State the preparation type.
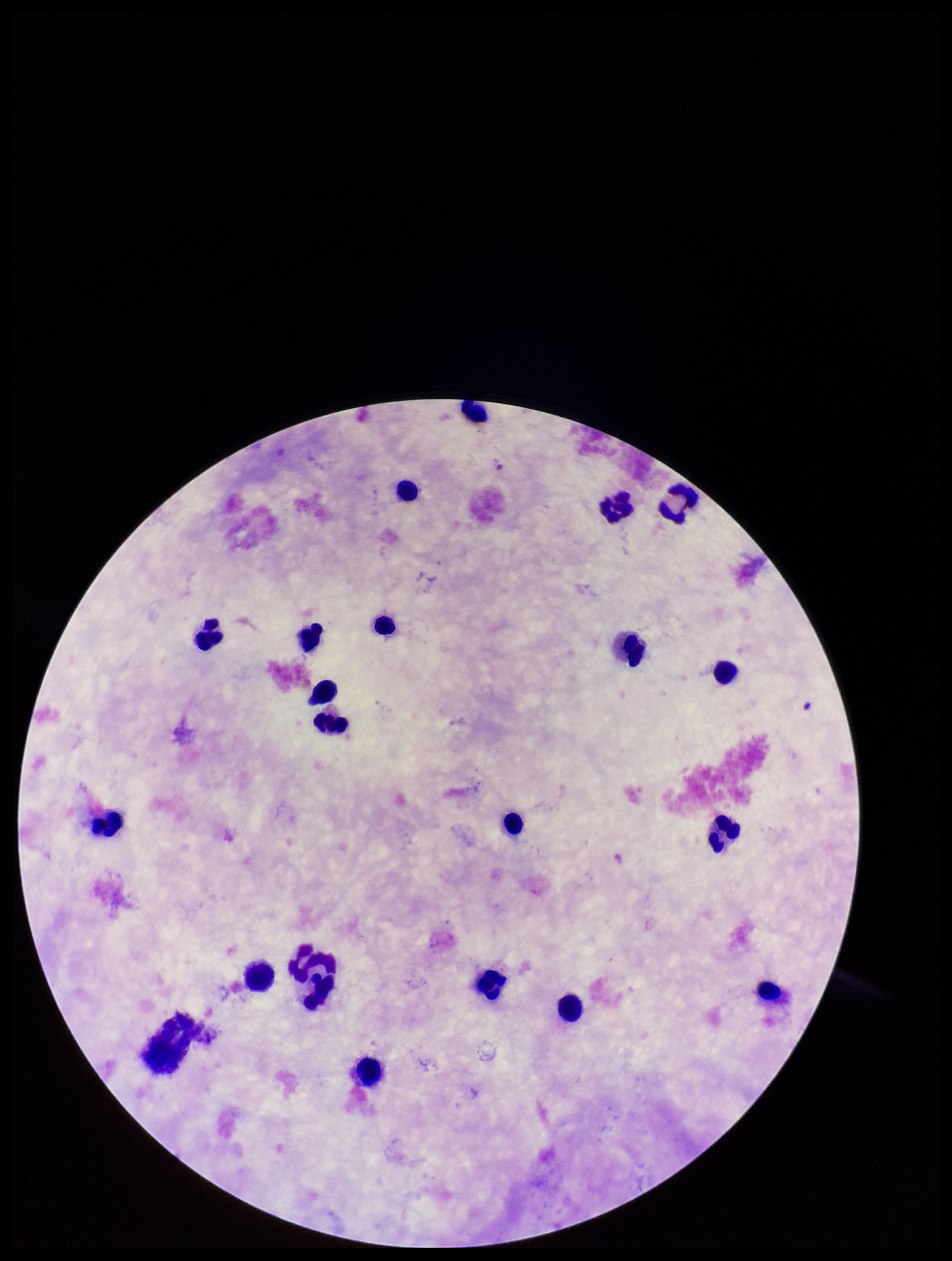
A thick smear.

Stained with Giemsa. Parasite count: 0. One field from this slide. Image is 952×1261 pixels. Photographed through the microscope eyepiece with a smartphone camera. Plasmodium parasites: none detected. Patient malaria status: negative. Leukocyte count: 21.